Report the malaria status of this cell.
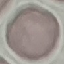

It is uninfected.

Photographed with a smartphone camera at the microscope eyepiece. Thin blood smear. Automatically extracted cell patch, resized to 64 × 64 pixels. Giemsa-stained preparation.